Classify this cell by malaria status.
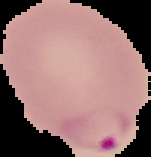
It is parasitized.

Summary:
  - Preparation: thin blood film
  - Image size: 151×157 pixels
  - Image type: cell region segmented out of the field of view; surrounding area masked to black